State which parasite is depicted.
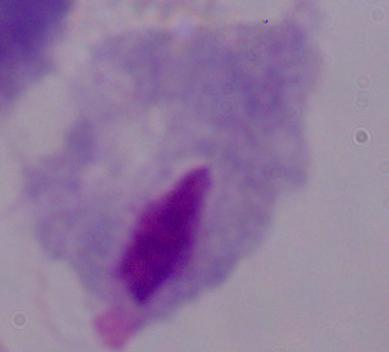

This is a trichomonad.

modality: micrograph
magnification: 1000x